Assess the morphology of the red blood cells.
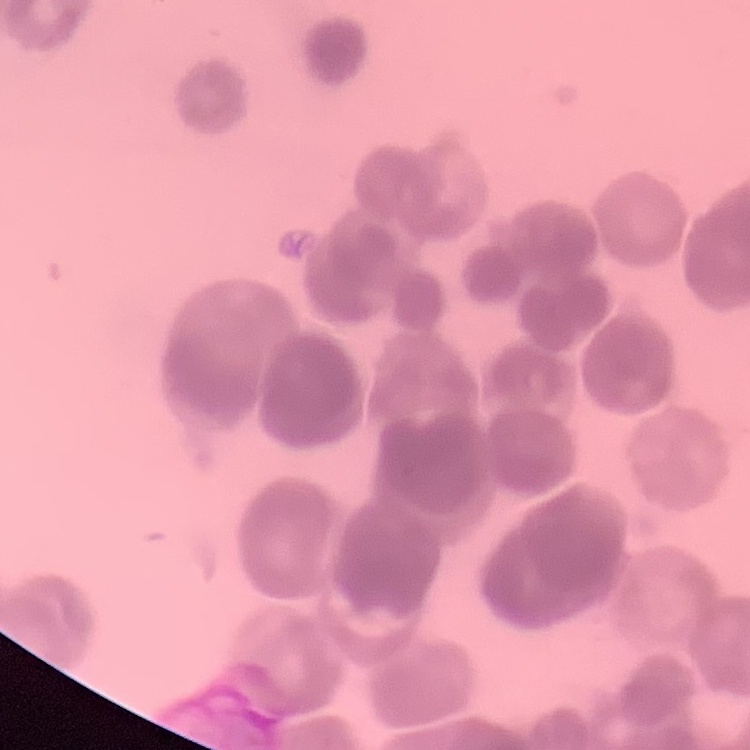

Rouleaux formation.

Summary:
  - Preparation: thin blood smear
  - Image type: one tile cut from a larger photomicrograph
  - Stain: Field's or Giemsa